Outline each blood parasite and name the species.
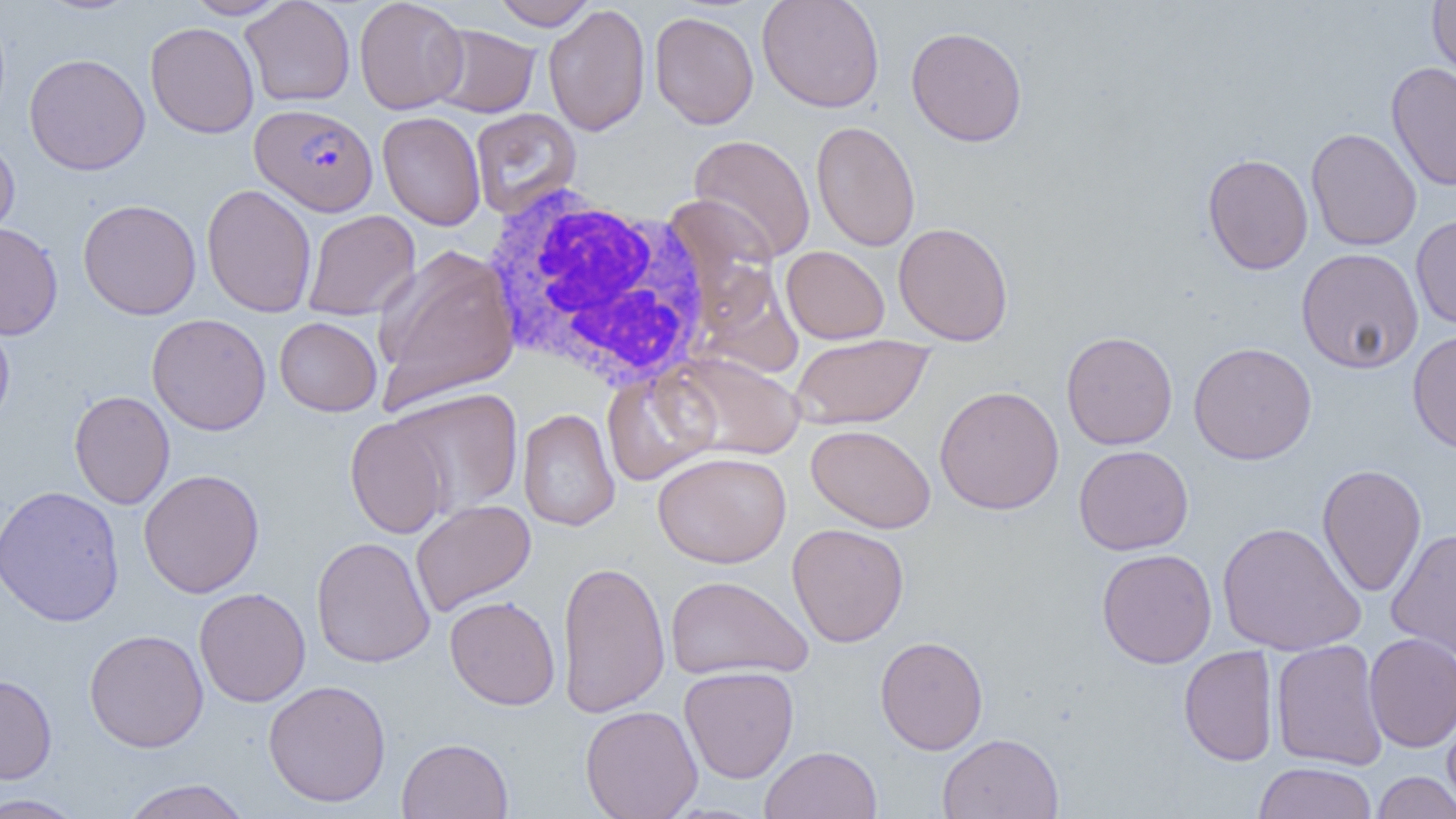

Approximate bounding boxes as (x1, y1, x2, y2) in pixels.
Plasmodium falciparum-infected red blood cells: (250, 103, 378, 217).
No Plasmodium ovale, Plasmodium malariae, Plasmodium vivax, Babesia divergens, or Trypanosoma brucei observed.

Summary:
  - Uninfected red blood cell locations: (35, 0, 141, 15), (183, 0, 290, 19), (240, 0, 355, 106), (354, 0, 469, 114), (490, 0, 598, 30), (757, 0, 885, 113), (1428, 0, 1456, 83), (543, 4, 651, 137), (649, 11, 759, 129), (145, 22, 259, 138), (429, 24, 541, 118), (905, 25, 1028, 146), (24, 53, 150, 175), (1386, 62, 1456, 190), (469, 108, 581, 218), (377, 111, 486, 230), (810, 120, 920, 252), (1306, 128, 1422, 251), (689, 134, 815, 262), (0, 136, 20, 247), (1202, 153, 1313, 275), (201, 184, 317, 318), (78, 199, 202, 320), (302, 209, 420, 321), (1410, 214, 1456, 330), (0, 222, 63, 340), (893, 222, 1014, 346), (372, 245, 520, 413), (781, 246, 889, 344), (1296, 247, 1424, 374), (147, 313, 271, 435), (0, 314, 15, 432), (274, 316, 382, 416), (1407, 329, 1456, 454), (1061, 330, 1178, 450), (790, 335, 934, 429), (1188, 342, 1318, 465), (668, 351, 805, 461), (600, 368, 720, 485), (934, 385, 1064, 515), (390, 387, 523, 517), (69, 390, 174, 509), (517, 408, 620, 532), (345, 416, 450, 539), (806, 424, 936, 533), (1073, 445, 1194, 555), (652, 451, 792, 568), (1317, 464, 1427, 597), (138, 469, 265, 598), (0, 484, 125, 628), (411, 498, 536, 616), (1217, 521, 1366, 656), (787, 523, 909, 647), (1386, 527, 1456, 662), (311, 536, 435, 668), (1096, 548, 1217, 668), (556, 560, 670, 718), (665, 575, 813, 681), (194, 587, 311, 707), (444, 596, 561, 710), (84, 628, 209, 753), (1364, 632, 1456, 752), (875, 635, 988, 754), (1271, 639, 1388, 770), (1178, 645, 1279, 766), (679, 666, 799, 783), (0, 673, 57, 784), (263, 679, 391, 807), (579, 705, 703, 818), (1442, 705, 1456, 812), (937, 732, 1064, 819), (397, 737, 513, 818), (760, 746, 883, 819), (1253, 761, 1378, 819), (1371, 771, 1456, 819), (119, 778, 252, 819), (0, 794, 86, 818)
  - White blood cell locations: (481, 183, 717, 391)
  - Slide-level diagnosis: Plasmodium falciparum
  - Modality: light microscopy
  - Preparation: thin blood smear
  - Field of view: single
  - Image size: 1456×819 pixels
  - Magnification: 1000x